Assess this cell for malaria.
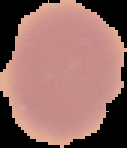

It is uninfected.

Summary:
  - Image size: 127×148 pixels
  - Preparation: thin blood smear
  - Image type: segmented cell region on a black background